Give the position of every leukocyte visible.
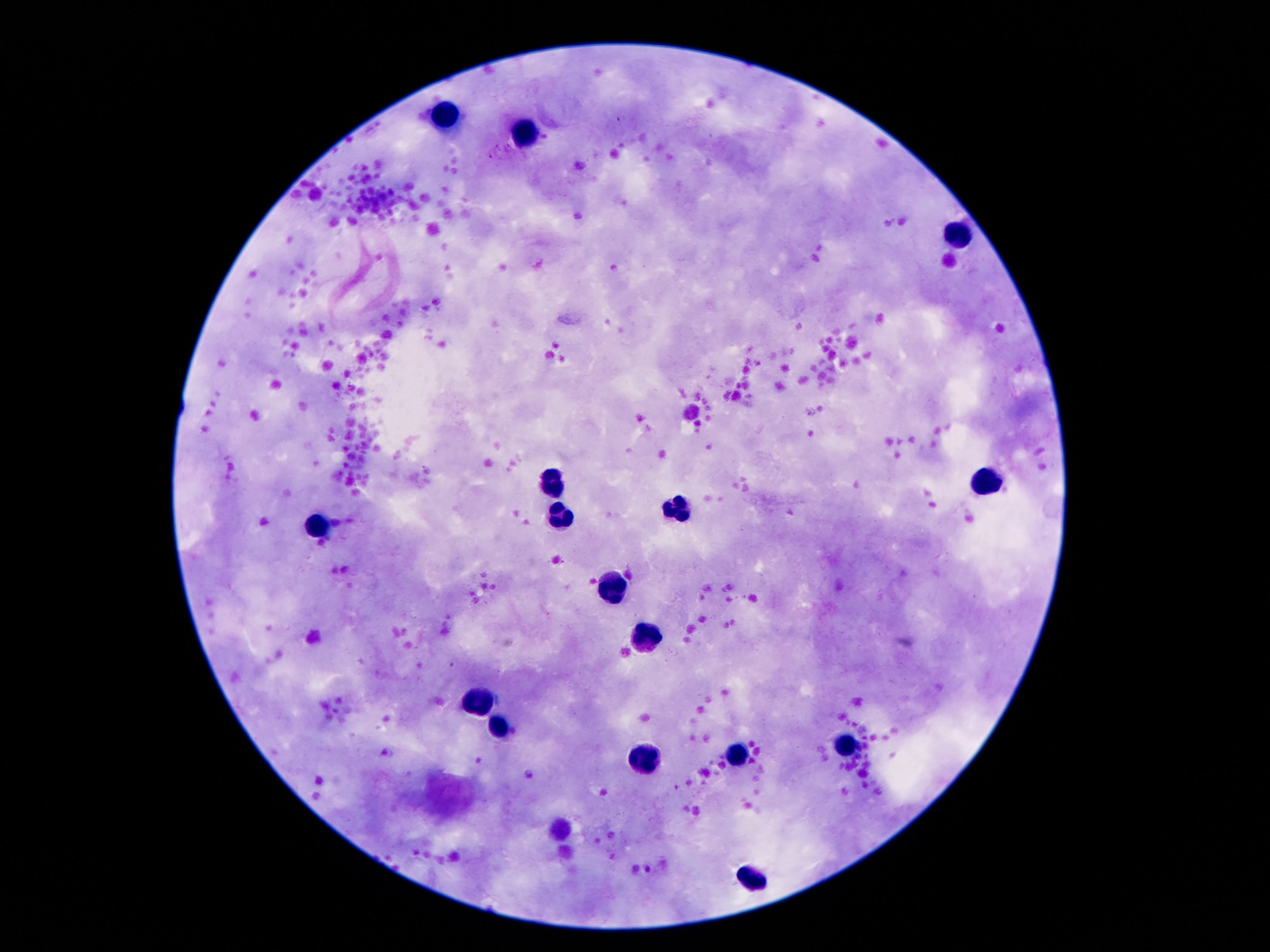
Approximate centers as [x, y] in pixels.
Leukocytes: [446, 114], [526, 129], [959, 235], [986, 483], [555, 484], [679, 507], [562, 514], [318, 528], [614, 588], [646, 635], [477, 703], [506, 728], [846, 744], [740, 750], [648, 762], [749, 877].

Summary:
  - Image size: 1270×952 pixels
  - Patient malaria status: negative
  - Field of view: single
  - Stain: Giemsa
  - Preparation: thick blood smear
  - Capture: smartphone camera through the microscope eyepiece
  - Magnification: 100x